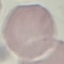 Result: negative for malaria parasites. Photographed with a smartphone camera at the microscope eyepiece. Automatically extracted cell patch, resized to 64 × 64 pixels. Giemsa-stained preparation. Thin blood film.